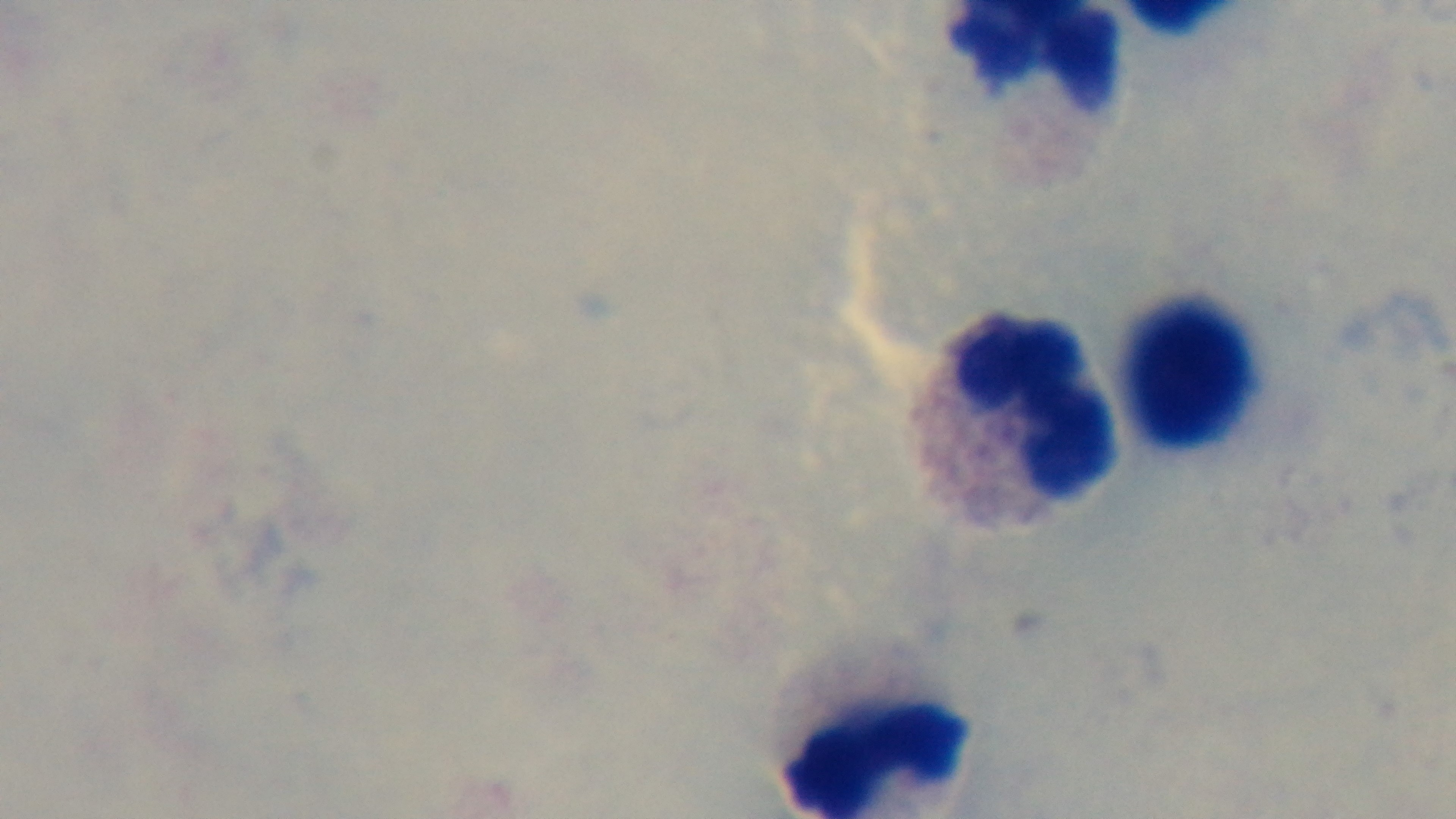 100x oil-immersion objective. Preparation: thick. One field from the slide. Light microscopy. Captured with a mounted 4K digital camera. Giemsa stain. Malaria status: negative.